Describe the morphology of the erythrocytes.
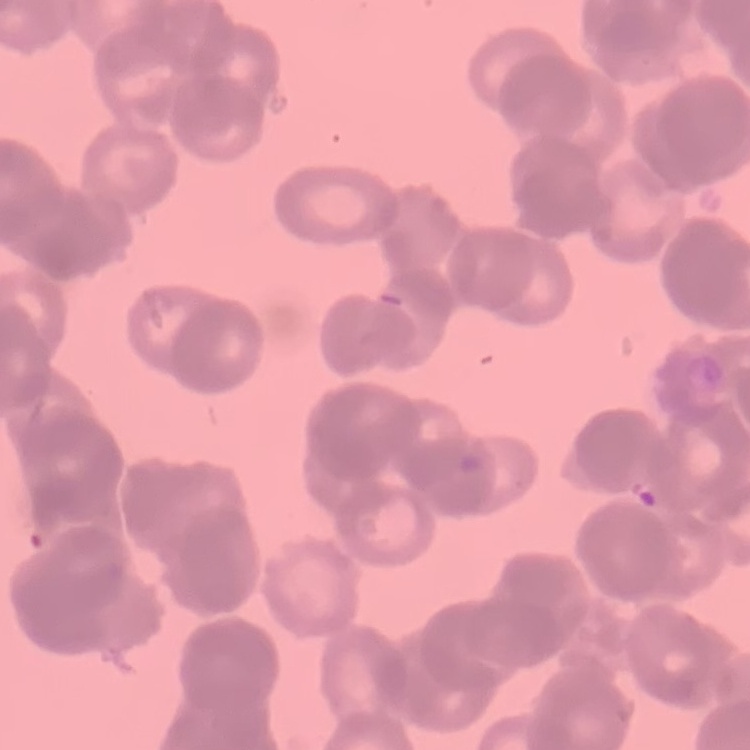
They show rouleaux formation.

preparation: thin peripheral smear
image_type: square crop of a larger photomicrograph
stain: Field's or Giemsa